Report the malaria status of this cell.
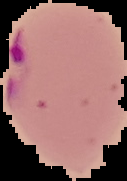
It is parasitized.

Segmented cell region on a black background. From a thin blood film. Image is 127×181 pixels.